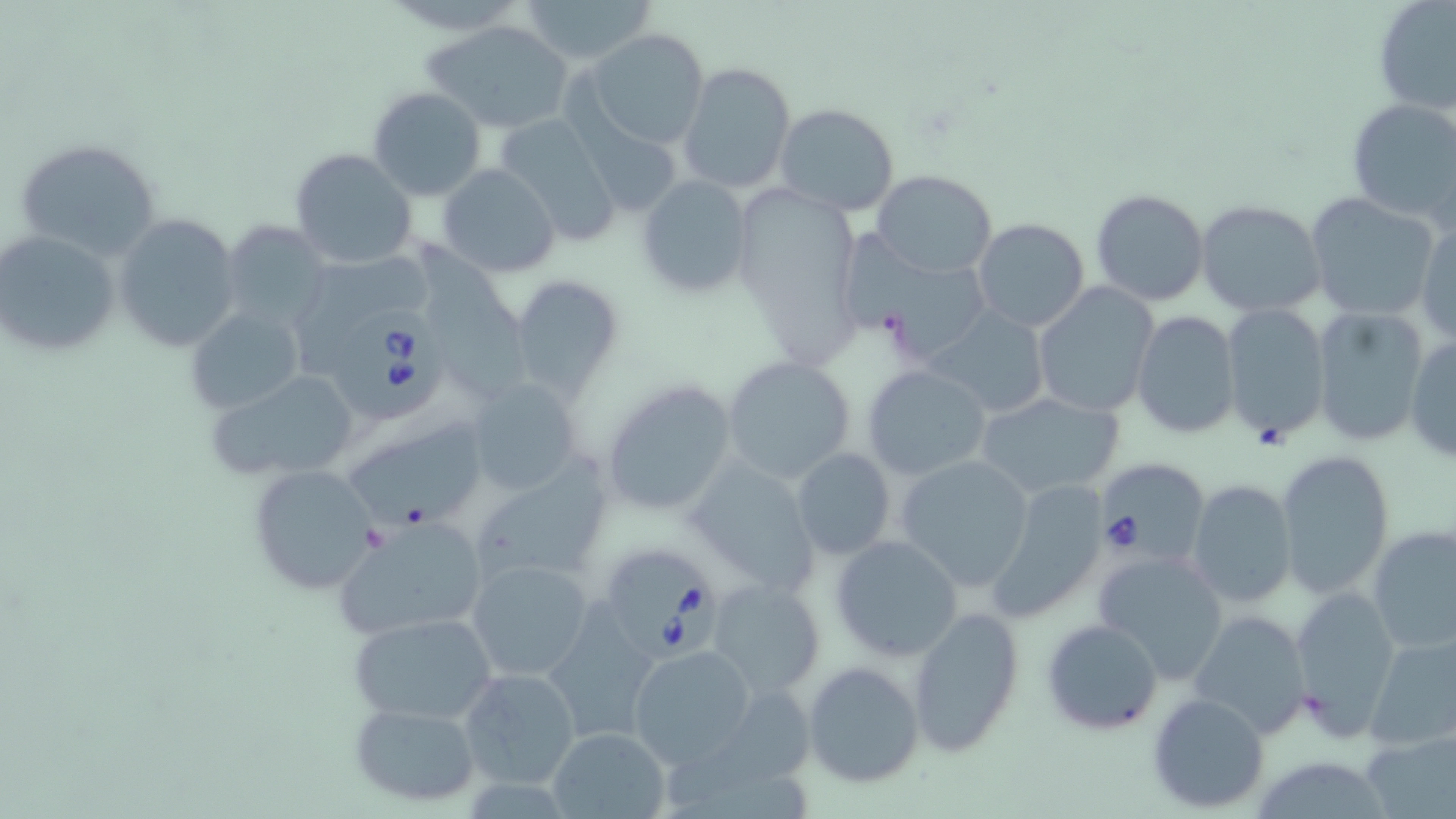

{
  "slide_level_diagnosis": "Babesia divergens",
  "image_size": "1456×819 pixels",
  "babesia_divergens_infected_red_blood_cell_locations": "approximate bounding boxes as [x1, y1, x2, y2] in pixels: [332, 301, 451, 423], [1095, 457, 1207, 566], [601, 547, 728, 666]",
  "uninfected_red_blood_cell_locations": "approximate bounding boxes as [x1, y1, x2, y2] in pixels: [521, 0, 654, 67], [1374, 0, 1456, 117], [422, 19, 577, 134], [586, 30, 711, 151], [679, 62, 796, 194], [368, 86, 486, 201], [1344, 99, 1456, 227], [774, 104, 901, 217], [494, 112, 625, 245], [15, 137, 162, 262], [288, 149, 417, 272], [437, 163, 561, 278], [872, 169, 998, 277], [637, 175, 755, 298], [745, 186, 877, 366], [1089, 187, 1210, 307], [1305, 193, 1441, 321], [1196, 198, 1327, 317], [111, 214, 240, 353], [1415, 216, 1456, 345], [972, 217, 1090, 332], [224, 222, 329, 330], [841, 230, 997, 357], [0, 231, 120, 356], [288, 239, 435, 343], [416, 240, 538, 408], [511, 273, 623, 401], [1032, 282, 1159, 417], [1220, 303, 1331, 442], [185, 306, 303, 416], [1311, 306, 1430, 449], [928, 309, 1048, 416], [1132, 310, 1240, 439], [1404, 332, 1455, 465], [722, 357, 855, 482], [860, 364, 990, 482], [204, 365, 363, 487], [600, 379, 738, 518], [465, 381, 585, 494], [971, 392, 1124, 499], [353, 420, 497, 531], [790, 448, 895, 560], [1275, 449, 1396, 599], [896, 454, 1035, 592], [685, 458, 823, 596], [470, 462, 614, 590], [247, 464, 381, 596], [982, 476, 1111, 622], [1187, 479, 1298, 609], [336, 518, 488, 641], [1366, 526, 1456, 653], [830, 534, 963, 662], [1093, 550, 1230, 684], [468, 558, 596, 682], [708, 578, 825, 697], [1060, 579, 1208, 718], [1287, 585, 1401, 737], [906, 605, 1026, 758], [1187, 609, 1314, 740], [349, 611, 499, 726], [1041, 617, 1164, 736], [1364, 629, 1456, 751], [629, 645, 756, 767], [804, 660, 925, 787], [458, 665, 582, 789], [1147, 692, 1270, 811], [350, 699, 482, 806], [546, 727, 671, 818], [1361, 729, 1454, 819]",
  "field_of_view": "single",
  "stain": "May-Grünwald-Giemsa",
  "magnification": "1000x",
  "modality": "light microscopy",
  "preparation": "thin blood smear"
}